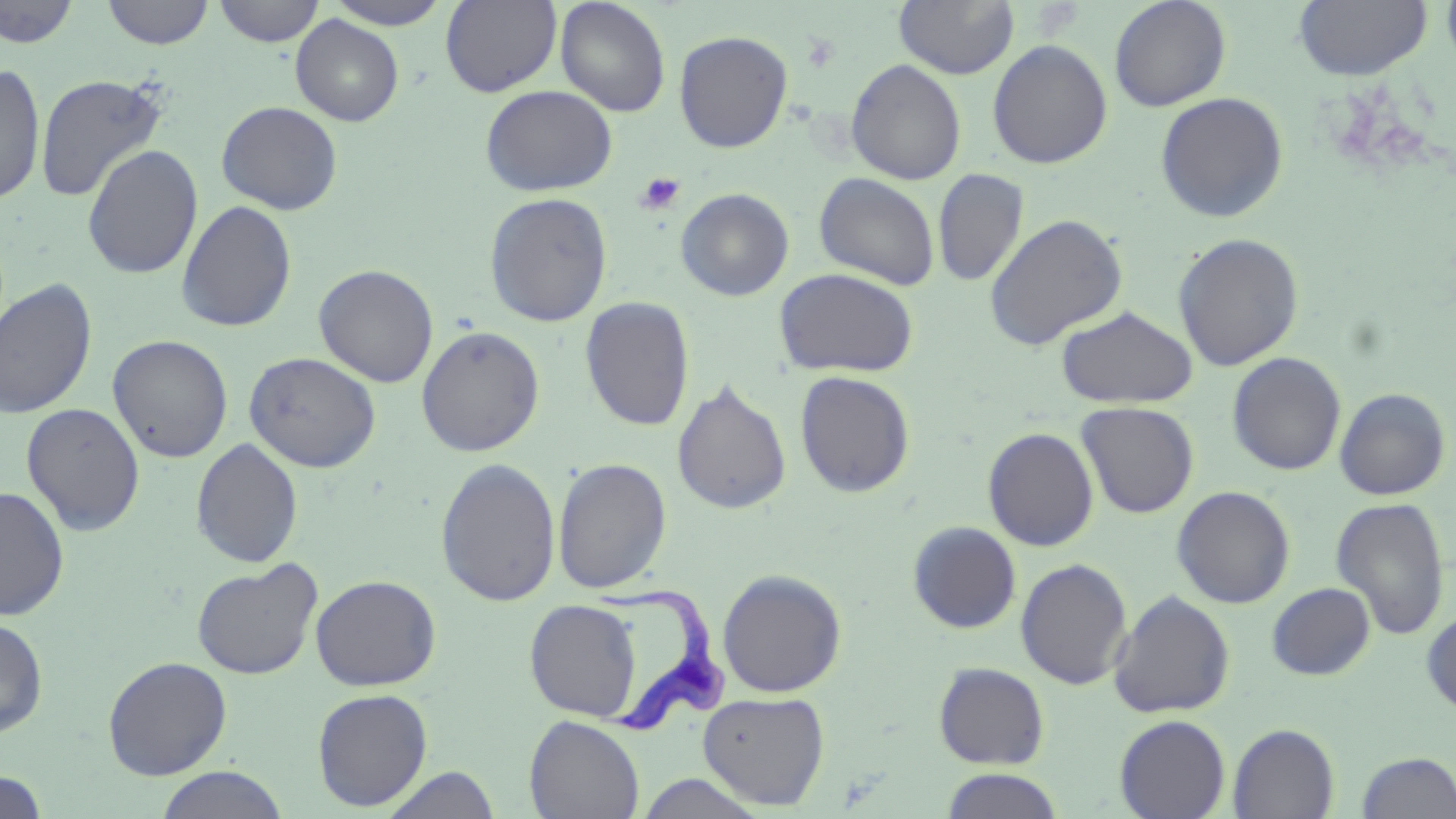
slide_level_diagnosis: Trypanosoma brucei
stain: May-Grünwald-Giemsa
platelet_locations: 'approximate bounding boxes as [x1, y1, x2, y2] in pixels: [635, 171, 686, 216]'
magnification: 1000x
trypanosoma_brucei_locations: 'approximate bounding boxes as [x1, y1, x2, y2] in pixels: [586, 580, 734, 737]'
modality: light microscopy
image_size: 1456×819 pixels
preparation: thin blood smear
uninfected_red_blood_cell_locations: 'approximate bounding boxes as [x1, y1, x2, y2] in pixels: [102, 0, 215, 49], [213, 0, 326, 47], [324, 0, 454, 29], [440, 0, 562, 96], [555, 0, 671, 117], [894, 0, 1019, 79], [1108, 0, 1232, 111], [1294, 0, 1432, 81], [1440, 0, 1456, 75], [0, 1, 82, 48], [290, 15, 404, 126], [673, 30, 793, 153], [988, 39, 1113, 169], [845, 59, 966, 185], [0, 63, 46, 205], [34, 73, 169, 203], [479, 85, 617, 196], [1154, 91, 1289, 223], [216, 101, 343, 214], [81, 144, 203, 280], [933, 168, 1029, 287], [814, 172, 940, 290], [675, 187, 794, 301], [483, 192, 613, 327], [176, 199, 297, 333], [984, 213, 1128, 350], [1172, 232, 1304, 371], [313, 264, 439, 387], [773, 267, 919, 378], [0, 278, 98, 420], [579, 297, 695, 432], [1055, 305, 1197, 408], [416, 325, 545, 457], [108, 334, 233, 463], [243, 351, 381, 473], [1227, 352, 1346, 476], [794, 370, 915, 498], [672, 381, 792, 514], [1334, 387, 1451, 500], [1076, 401, 1199, 518], [21, 402, 146, 536], [982, 427, 1099, 551], [190, 438, 304, 568], [435, 457, 562, 607], [553, 457, 672, 594], [0, 485, 70, 621], [1171, 485, 1295, 608], [1330, 497, 1450, 641], [907, 521, 1022, 634], [192, 558, 323, 679], [1015, 558, 1133, 690], [716, 568, 847, 697], [310, 574, 441, 691], [1266, 582, 1376, 680], [1108, 589, 1236, 719], [524, 598, 643, 722], [1421, 607, 1456, 717], [0, 617, 49, 738], [102, 656, 232, 780], [933, 662, 1050, 769], [311, 687, 434, 810], [697, 690, 831, 810], [524, 714, 645, 819], [1114, 714, 1231, 819], [1228, 724, 1340, 819], [1356, 751, 1455, 818], [154, 766, 291, 819], [381, 766, 502, 819], [940, 769, 1067, 819], [0, 771, 50, 817], [634, 772, 767, 817]'
field_of_view: single